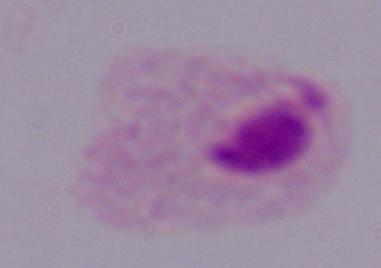
Summary:
  - Magnification: 1000x
  - Modality: photomicrograph
  - Identification: trichomonad